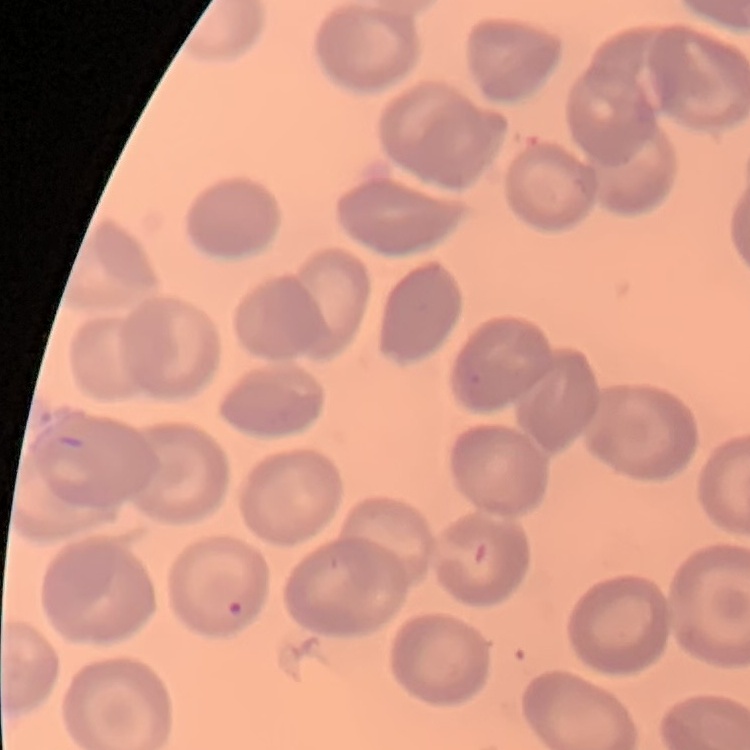

Summary:
  - Erythrocyte morphology: no rouleaux formation
  - Preparation: thin blood film
  - Stain: Field's or Giemsa
  - Image type: square crop of a larger photomicrograph